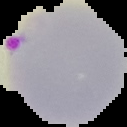

image_size: 127×127 pixels
result: Plasmodium parasites identified
image_type: segmented cell region on a black background
preparation: thin blood smear